Outline each Plasmodium falciparum-infected red blood cell.
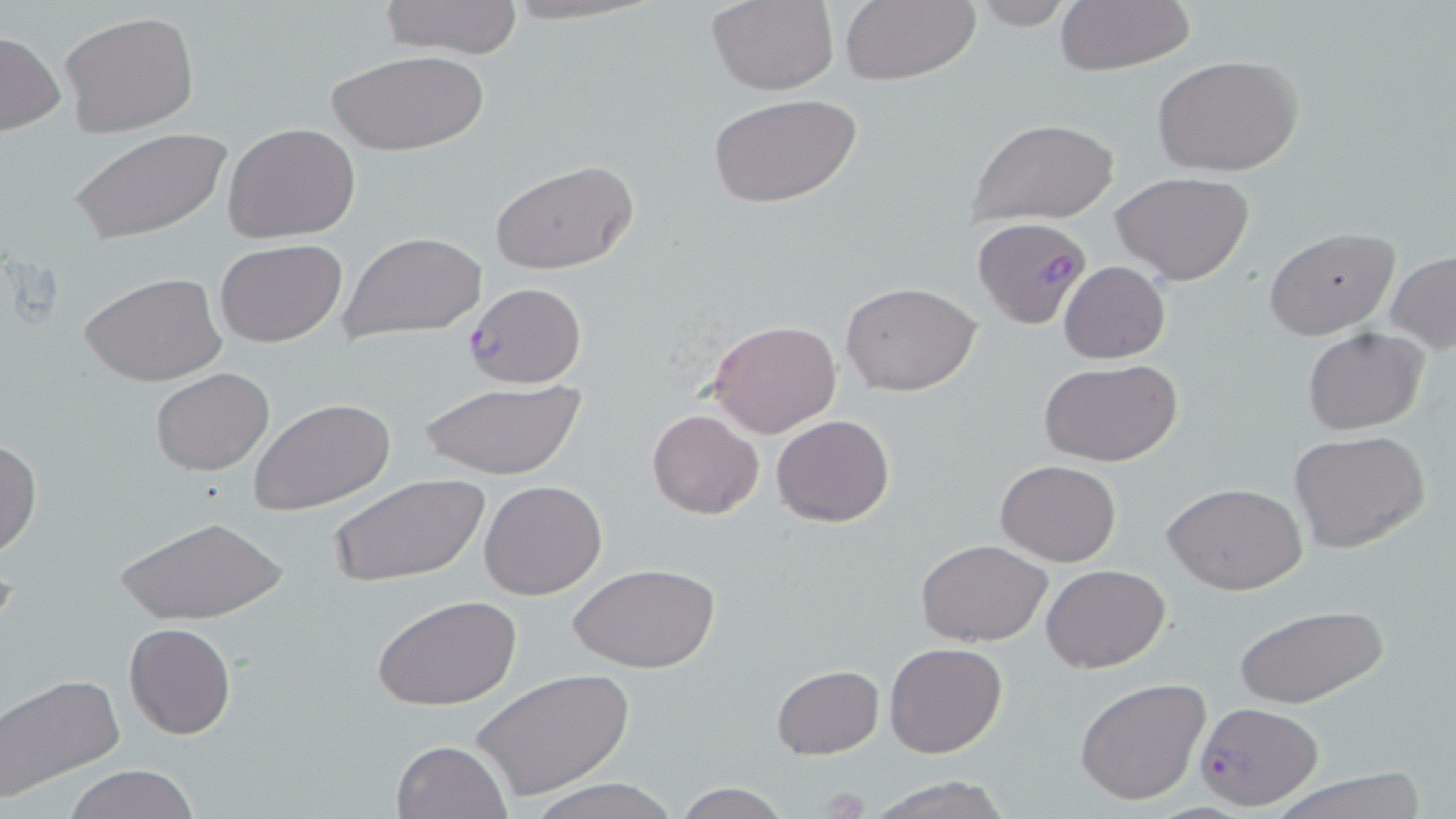

Approximate bounding boxes as (x1,y1)-(x2,y2) corner pairs in pixels.
Plasmodium falciparum-infected red blood cells: (973,218)-(1090,330), (463,282)-(587,388), (1194,702)-(1324,808).

Uninfected red blood cell locations: (378,0)-(524,58), (969,0)-(1077,30), (1053,0)-(1194,77), (705,1)-(839,94), (838,1)-(981,87), (60,12)-(201,136), (0,31)-(64,136), (327,48)-(488,156), (1153,55)-(1304,177), (706,93)-(864,210), (965,117)-(1120,225), (223,123)-(362,244), (68,127)-(232,244), (490,161)-(636,276), (1110,172)-(1253,283), (1265,227)-(1400,339), (339,231)-(486,341), (214,239)-(346,348), (1386,250)-(1456,356), (1059,261)-(1170,364), (81,273)-(226,388), (840,280)-(982,395), (709,319)-(841,438), (1304,328)-(1428,435), (1040,359)-(1182,466), (149,366)-(274,476), (417,378)-(589,481), (249,397)-(396,517), (646,409)-(764,520), (771,413)-(895,527), (1290,430)-(1431,554), (0,438)-(42,557), (995,460)-(1121,567), (330,472)-(487,590), (480,479)-(607,600), (1162,481)-(1308,596), (112,514)-(287,623), (916,539)-(1052,647), (570,564)-(718,674), (1042,565)-(1167,673), (374,595)-(519,711), (1233,604)-(1389,711), (124,621)-(235,740), (884,642)-(1007,758), (771,664)-(884,759), (471,668)-(633,801), (1,673)-(127,801), (1075,677)-(1211,806), (391,739)-(511,819), (62,764)-(200,819), (1271,768)-(1430,819), (863,773)-(1012,819), (528,778)-(681,819), (671,782)-(795,818). Slide-level diagnosis: Plasmodium falciparum. Image is 1456×819 pixels. Thin blood smear. Light microscopy. One field of a larger specimen. May-Grünwald-Giemsa stain. 1000x magnification.